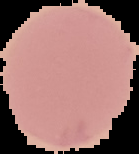
image_size: 139×154 pixels
malaria_status: uninfected
preparation: thin blood smear
image_type: segmented cell region with the area outside set to black